Give the preparation type.
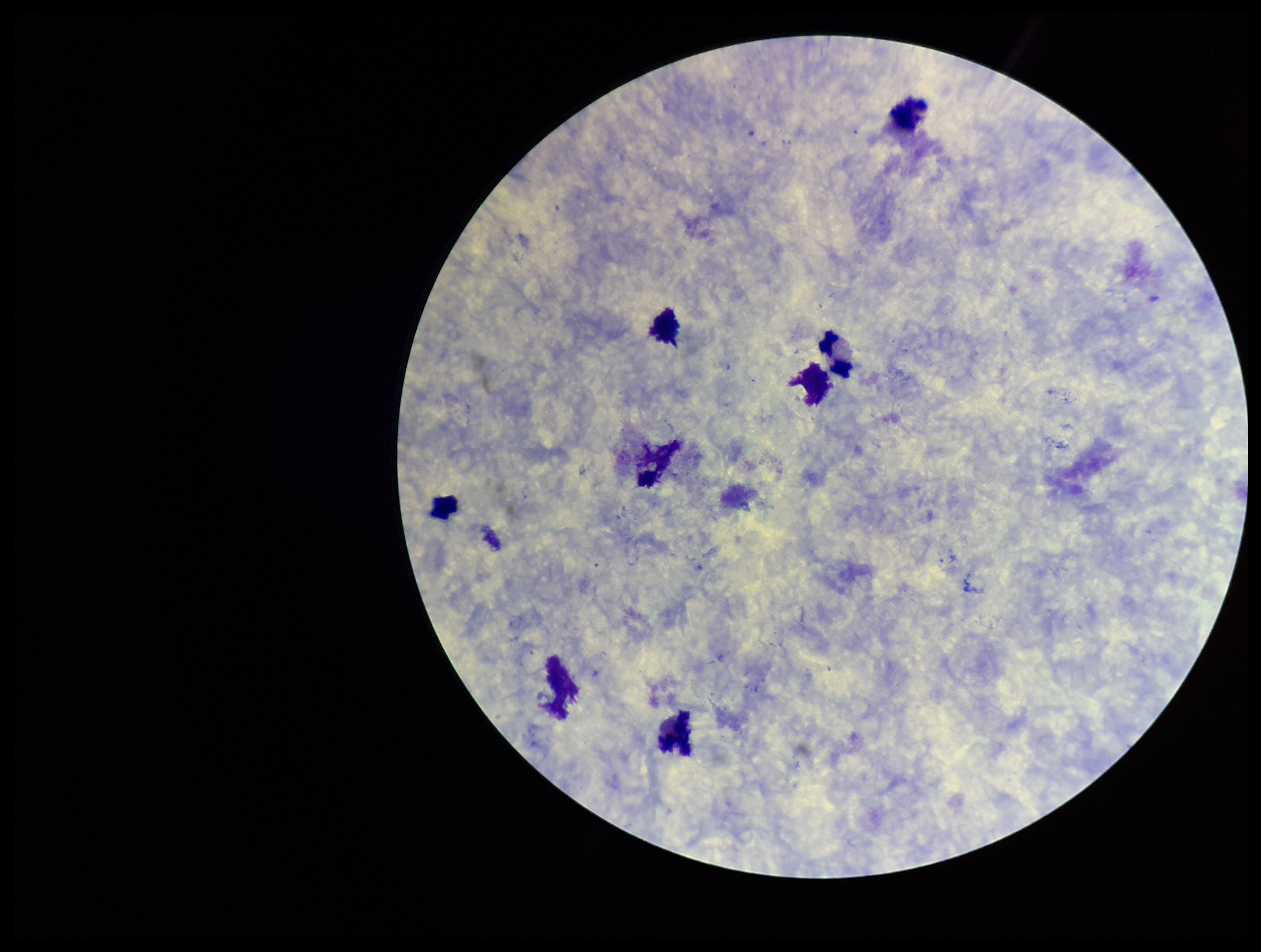

It is a thick blood smear.

image size = 1261×952 pixels
field of view = single
Plasmodium parasites = none detected
parasite count = 0
capture = smartphone photograph through the microscope eyepiece
stain = Giemsa
leukocyte count = 8
patient malaria status = negative